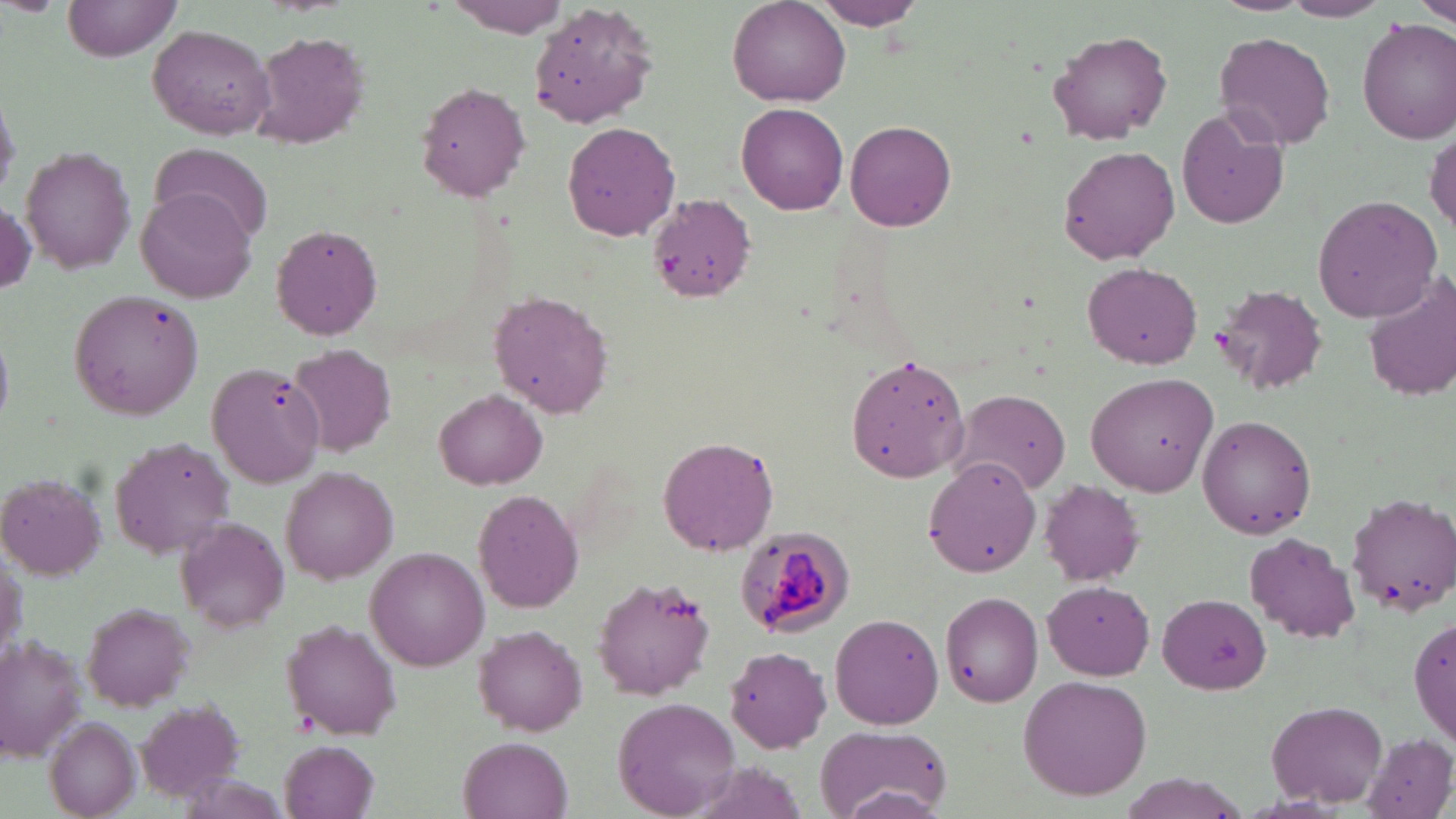

Approximate bounding boxes as (x1, y1, x2, y2) in pixels. Plasmodium malariae-infected red blood cell locations: (734, 526, 855, 640). Uninfected red blood cell locations: (63, 0, 182, 60), (812, 0, 923, 30), (1211, 0, 1312, 15), (1416, 0, 1456, 30), (440, 1, 573, 38), (1279, 1, 1392, 22), (728, 2, 851, 108), (1358, 20, 1456, 142), (147, 25, 275, 139), (1045, 28, 1175, 143), (250, 30, 372, 149), (1215, 31, 1335, 150), (416, 80, 532, 202), (0, 84, 20, 204), (736, 102, 849, 216), (1175, 107, 1288, 230), (845, 120, 955, 232), (563, 121, 681, 242), (1427, 126, 1456, 236), (152, 142, 273, 243), (1058, 145, 1180, 262), (21, 146, 138, 273), (135, 189, 258, 304), (1311, 194, 1442, 322), (649, 195, 756, 303), (1, 201, 35, 298), (271, 223, 384, 341), (1080, 261, 1203, 369), (1364, 271, 1456, 402), (1211, 284, 1329, 396), (489, 291, 615, 419), (0, 329, 13, 432), (288, 342, 399, 459), (844, 354, 971, 483), (1086, 373, 1218, 496), (434, 388, 547, 489), (951, 389, 1072, 495), (1196, 414, 1318, 539), (110, 435, 237, 557), (657, 435, 780, 556), (923, 458, 1041, 580), (282, 468, 398, 583), (0, 473, 108, 580), (1038, 479, 1145, 586), (472, 489, 584, 613), (1347, 493, 1456, 616), (174, 515, 291, 632), (1244, 533, 1359, 644), (0, 545, 26, 668), (366, 547, 491, 670), (590, 574, 718, 700), (1043, 580, 1158, 678), (939, 590, 1044, 707), (1156, 592, 1271, 694), (82, 601, 194, 709), (1409, 611, 1456, 749), (829, 613, 944, 729), (283, 620, 403, 741), (474, 623, 587, 735), (0, 632, 85, 759), (725, 646, 834, 753), (1018, 673, 1153, 801), (612, 697, 740, 816), (1267, 699, 1391, 807), (135, 700, 249, 804), (45, 717, 140, 818), (814, 724, 951, 819), (1361, 733, 1455, 819), (460, 735, 575, 819), (279, 740, 380, 819), (677, 760, 813, 819), (1115, 774, 1249, 818). Slide-level diagnosis: Plasmodium malariae. Optical microscopy. May-Grünwald-Giemsa stain. Thin blood film. One field of a larger specimen. Image is 1456×819 pixels. Captured at 1000x magnification.